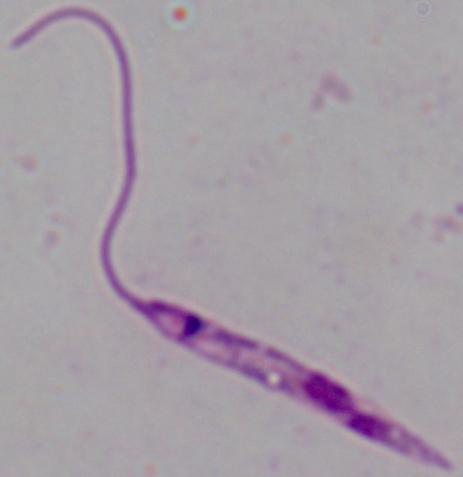
Captured at 1000x magnification. A Leishmania parasite is shown. Photomicrograph.